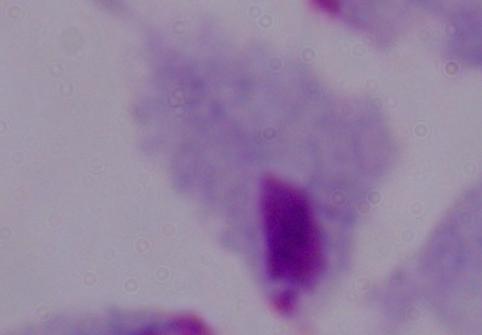

Photomicrograph. Captured at 1000x magnification. A trichomonad is seen.